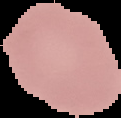
Summary:
  - Image size: 121×118 pixels
  - Image type: segmented cell region on a black background
  - Malaria status: uninfected
  - Preparation: thin blood smear